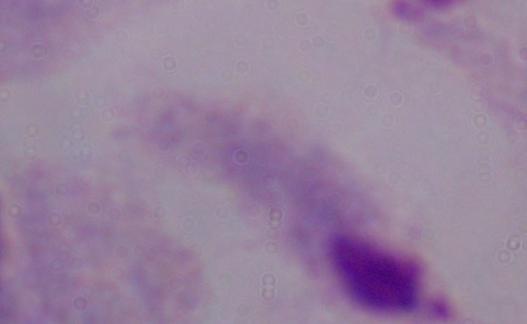

Photomicrograph. A trichomonad is shown. Captured at 1000x magnification.